Point out each leukocyte.
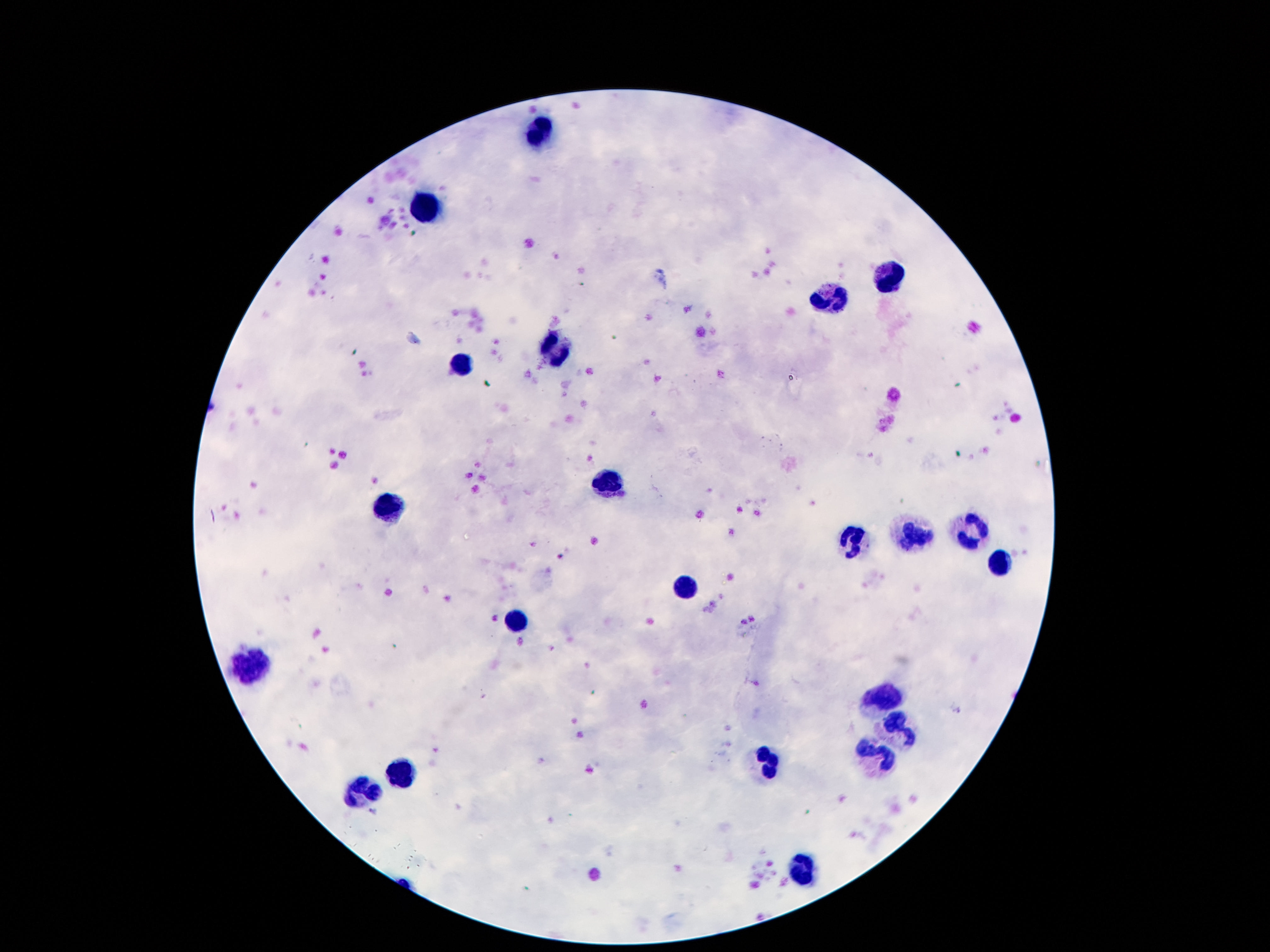
Approximate centers as [x, y] in pixels.
Leukocytes: [540, 132], [422, 209], [895, 278], [829, 297], [554, 347], [461, 359], [611, 483], [386, 504], [970, 530], [913, 537], [852, 542], [999, 562], [686, 586], [513, 621], [254, 667], [886, 699], [897, 725], [879, 757], [768, 763], [402, 770], [363, 792], [802, 869].

Thick blood film. Image is 1270×952 pixels. Patient malaria status: uninfected. 100x magnification. Single field of view. Photographed through the microscope eyepiece with a smartphone camera. Giemsa-stained preparation.